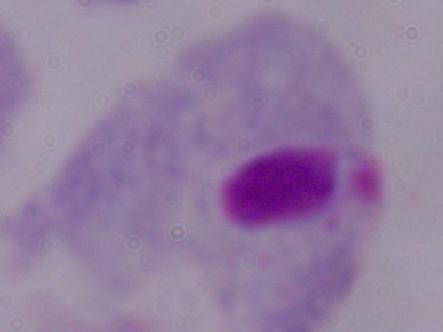

Micrograph. Captured at 1000x magnification. A trichomonad is seen.